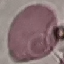
Malaria status: uninfected. Photographed with a smartphone camera at the microscope eyepiece. Cell patch, automatically extracted from a larger field of view and resized to 64 × 64 pixels. Thin blood film. Giemsa stain.